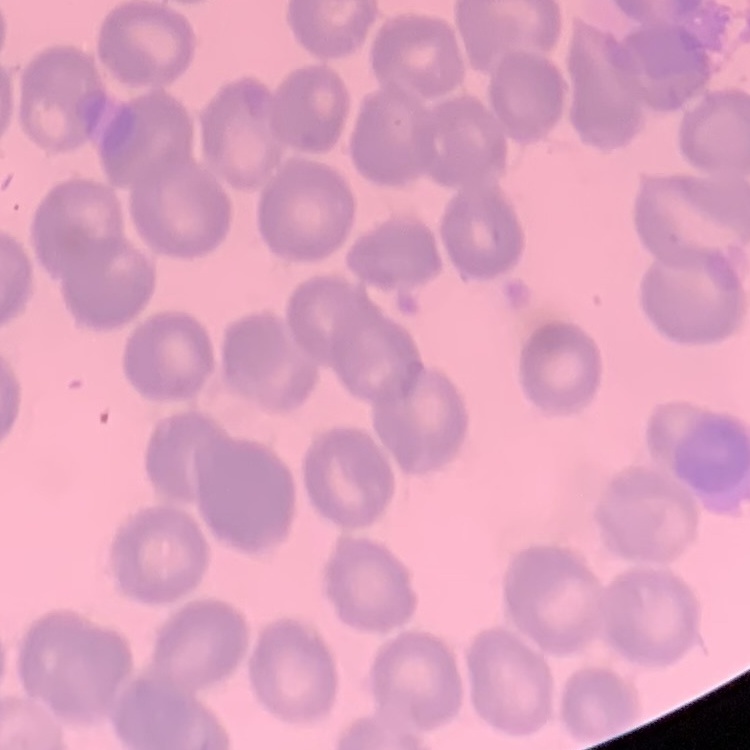
The red blood cells show no rouleaux formation. Field's or Giemsa stain. Square crop of a larger photomicrograph. Thin blood smear.